Identify the parasite.
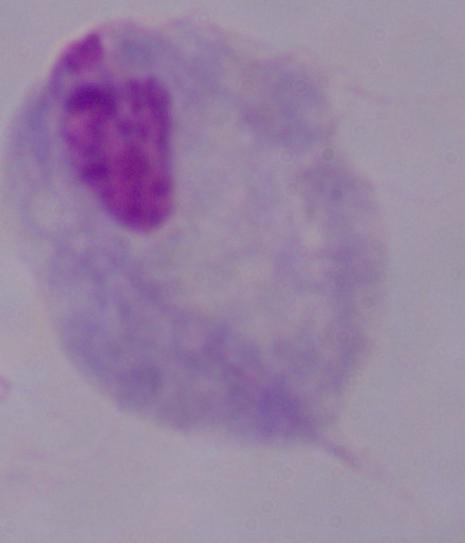
A trichomonad.

Summary:
  - Magnification: 1000x
  - Modality: micrograph